Name the parasite shown.
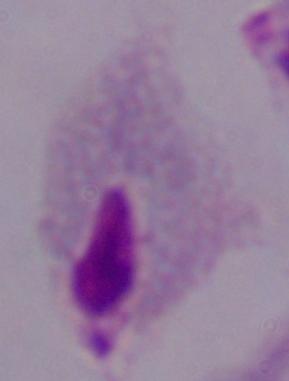
A trichomonad.

Captured at 1000x magnification. Photomicrograph.